State which parasite is depicted.
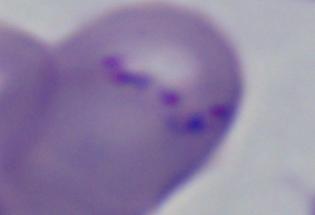

Babesia.

1000x magnification. Micrograph.